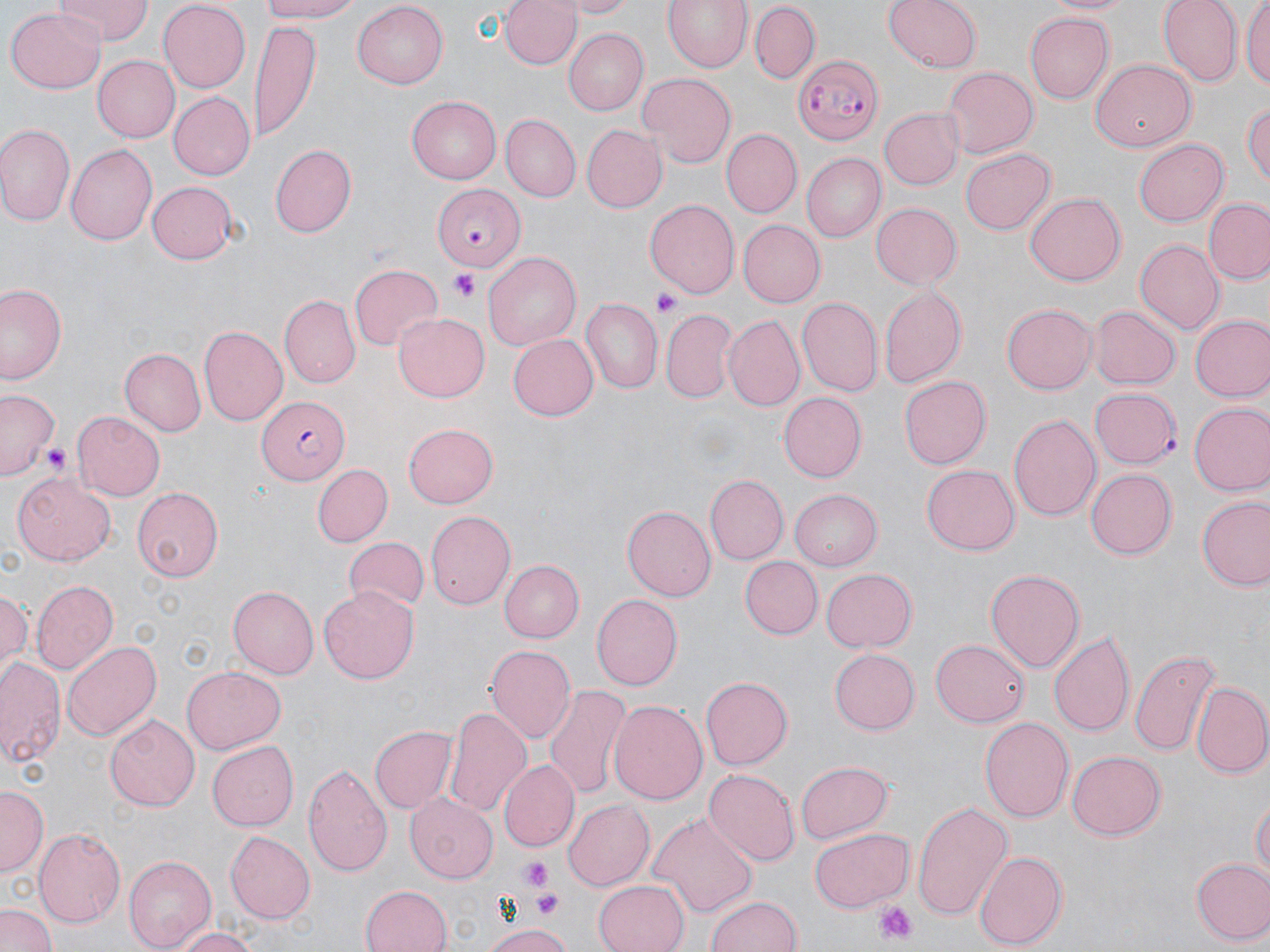
{
  "slide_level_diagnosis": "Plasmodium falciparum",
  "preparation": "thin blood film",
  "magnification": "1000x",
  "platelet_locations": "approximate bounding boxes as named x1/y1/x2/y2 corners in pixels: (x1=447, y1=272, x2=480, y2=301), (x1=652, y1=291, x2=679, y2=315), (x1=39, y1=440, x2=71, y2=473), (x1=520, y1=859, x2=552, y2=891), (x1=532, y1=890, x2=564, y2=920), (x1=873, y1=901, x2=920, y2=945)",
  "stain": "May-Grünwald-Giemsa",
  "modality": "light microscopy",
  "plasmodium_falciparum_infected_red_blood_cell_locations": "approximate bounding boxes as named x1/y1/x2/y2 corners in pixels: (x1=795, y1=53, x2=883, y2=143), (x1=434, y1=181, x2=525, y2=269), (x1=255, y1=398, x2=349, y2=484)",
  "image_size": "1270×952 pixels",
  "uninfected_red_blood_cell_locations": "approximate bounding boxes as named x1/y1/x2/y2 corners in pixels: (x1=58, y1=0, x2=151, y2=45), (x1=254, y1=0, x2=368, y2=23), (x1=498, y1=0, x2=580, y2=72), (x1=561, y1=0, x2=636, y2=17), (x1=662, y1=0, x2=751, y2=74), (x1=883, y1=0, x2=981, y2=73), (x1=1040, y1=0, x2=1140, y2=17), (x1=1157, y1=0, x2=1242, y2=87), (x1=1242, y1=0, x2=1270, y2=93), (x1=157, y1=3, x2=250, y2=90), (x1=352, y1=3, x2=449, y2=88), (x1=749, y1=3, x2=820, y2=82), (x1=7, y1=4, x2=105, y2=91), (x1=1025, y1=11, x2=1115, y2=103), (x1=249, y1=24, x2=320, y2=141), (x1=566, y1=27, x2=650, y2=115), (x1=91, y1=55, x2=179, y2=142), (x1=1089, y1=60, x2=1195, y2=152), (x1=942, y1=65, x2=1038, y2=157), (x1=641, y1=74, x2=736, y2=166), (x1=168, y1=92, x2=255, y2=180), (x1=405, y1=96, x2=500, y2=185), (x1=1242, y1=100, x2=1270, y2=189), (x1=878, y1=107, x2=962, y2=189), (x1=503, y1=113, x2=580, y2=202), (x1=0, y1=123, x2=74, y2=226), (x1=580, y1=124, x2=667, y2=212), (x1=722, y1=130, x2=801, y2=216), (x1=1134, y1=137, x2=1228, y2=226), (x1=269, y1=144, x2=354, y2=237), (x1=67, y1=146, x2=156, y2=245), (x1=961, y1=147, x2=1055, y2=235), (x1=804, y1=153, x2=885, y2=242), (x1=145, y1=182, x2=240, y2=264), (x1=1024, y1=193, x2=1124, y2=284), (x1=1205, y1=198, x2=1270, y2=284), (x1=644, y1=200, x2=739, y2=298), (x1=871, y1=202, x2=961, y2=289), (x1=741, y1=219, x2=825, y2=306), (x1=1136, y1=241, x2=1223, y2=332), (x1=484, y1=249, x2=581, y2=348), (x1=350, y1=264, x2=442, y2=350), (x1=0, y1=285, x2=68, y2=387), (x1=879, y1=286, x2=966, y2=390), (x1=283, y1=294, x2=362, y2=388), (x1=797, y1=297, x2=881, y2=395), (x1=582, y1=300, x2=662, y2=394), (x1=1001, y1=300, x2=1097, y2=396), (x1=1090, y1=304, x2=1180, y2=390), (x1=661, y1=309, x2=737, y2=403), (x1=393, y1=312, x2=491, y2=402), (x1=1189, y1=314, x2=1270, y2=402), (x1=725, y1=315, x2=803, y2=409), (x1=200, y1=326, x2=287, y2=427), (x1=506, y1=334, x2=597, y2=421), (x1=120, y1=348, x2=206, y2=436), (x1=897, y1=374, x2=991, y2=470), (x1=1089, y1=384, x2=1181, y2=467), (x1=0, y1=388, x2=60, y2=480), (x1=778, y1=392, x2=866, y2=482), (x1=1188, y1=400, x2=1270, y2=494), (x1=72, y1=410, x2=166, y2=502), (x1=1008, y1=411, x2=1102, y2=525), (x1=403, y1=422, x2=498, y2=508), (x1=311, y1=464, x2=391, y2=548), (x1=922, y1=465, x2=1020, y2=556), (x1=1086, y1=470, x2=1176, y2=559), (x1=10, y1=472, x2=115, y2=566), (x1=706, y1=475, x2=789, y2=564), (x1=133, y1=487, x2=223, y2=581), (x1=789, y1=488, x2=882, y2=569), (x1=1197, y1=496, x2=1270, y2=590), (x1=622, y1=505, x2=716, y2=601), (x1=425, y1=510, x2=515, y2=610), (x1=343, y1=538, x2=428, y2=616), (x1=499, y1=556, x2=584, y2=643), (x1=741, y1=556, x2=822, y2=639), (x1=822, y1=567, x2=917, y2=652), (x1=985, y1=568, x2=1086, y2=673), (x1=30, y1=581, x2=117, y2=675), (x1=1, y1=585, x2=32, y2=677), (x1=228, y1=586, x2=318, y2=678), (x1=319, y1=587, x2=420, y2=685), (x1=592, y1=593, x2=682, y2=691), (x1=1049, y1=630, x2=1134, y2=736), (x1=930, y1=639, x2=1029, y2=726), (x1=63, y1=640, x2=159, y2=740), (x1=485, y1=646, x2=576, y2=744), (x1=1130, y1=647, x2=1222, y2=756), (x1=832, y1=648, x2=919, y2=734), (x1=0, y1=656, x2=65, y2=771), (x1=180, y1=668, x2=284, y2=754), (x1=700, y1=675, x2=790, y2=770), (x1=1191, y1=682, x2=1270, y2=777), (x1=544, y1=684, x2=629, y2=798), (x1=608, y1=700, x2=707, y2=805), (x1=445, y1=706, x2=530, y2=815), (x1=105, y1=714, x2=200, y2=812), (x1=979, y1=715, x2=1074, y2=825), (x1=370, y1=723, x2=456, y2=813), (x1=208, y1=741, x2=301, y2=831), (x1=1067, y1=750, x2=1166, y2=841), (x1=498, y1=760, x2=580, y2=851), (x1=796, y1=760, x2=893, y2=844), (x1=301, y1=761, x2=392, y2=877), (x1=705, y1=769, x2=798, y2=868), (x1=1, y1=786, x2=46, y2=877), (x1=405, y1=793, x2=498, y2=885), (x1=1252, y1=793, x2=1269, y2=886), (x1=562, y1=799, x2=654, y2=891), (x1=912, y1=801, x2=1012, y2=921), (x1=651, y1=811, x2=757, y2=919), (x1=34, y1=827, x2=125, y2=927), (x1=809, y1=827, x2=913, y2=912), (x1=227, y1=830, x2=315, y2=925), (x1=975, y1=848, x2=1067, y2=951), (x1=122, y1=855, x2=214, y2=951), (x1=1191, y1=856, x2=1270, y2=945), (x1=592, y1=880, x2=689, y2=952), (x1=359, y1=884, x2=453, y2=952), (x1=706, y1=894, x2=802, y2=952), (x1=0, y1=904, x2=57, y2=952), (x1=481, y1=922, x2=574, y2=952), (x1=169, y1=927, x2=262, y2=952)",
  "field_of_view": "single"
}